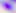
identification = Toxoplasma gondii
modality = micrograph
magnification = 400x